Identify the parasite.
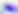

Toxoplasma gondii.

Micrograph. 400x magnification.